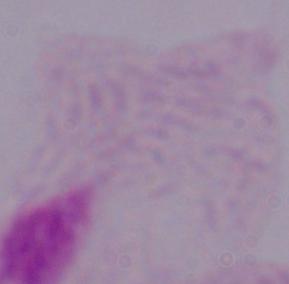 A trichomonad is seen. Photomicrograph. 1000x magnification.